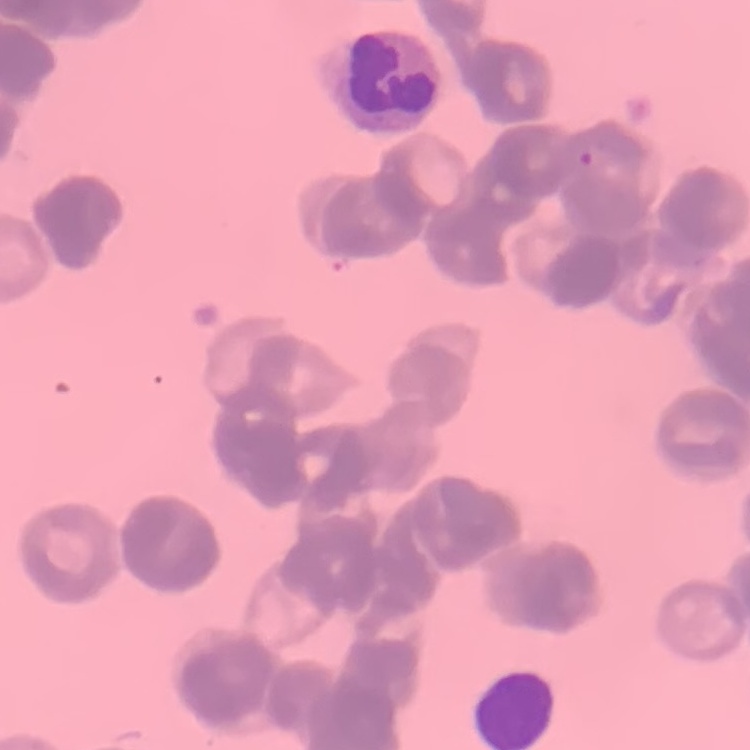

{
  "red_blood_cell_morphology": "rouleaux formation",
  "image_type": "one tile cut from a larger photomicrograph",
  "stain": "Field's or Giemsa",
  "preparation": "thin blood smear"
}